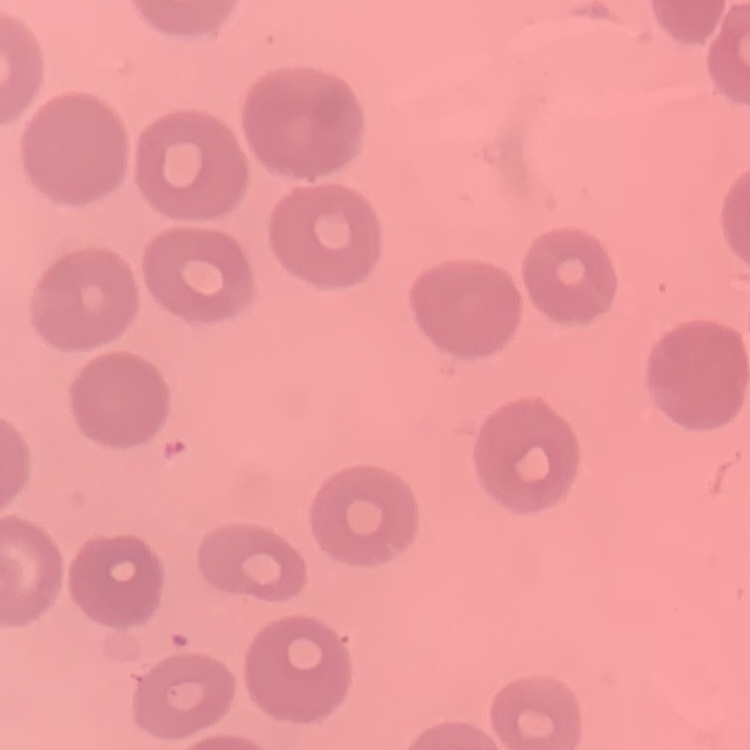
Summary:
  - Red blood cell morphology: no rouleaux formation
  - Preparation: thin blood film
  - Stain: Field's or Giemsa
  - Image type: one tile cut from a larger photomicrograph